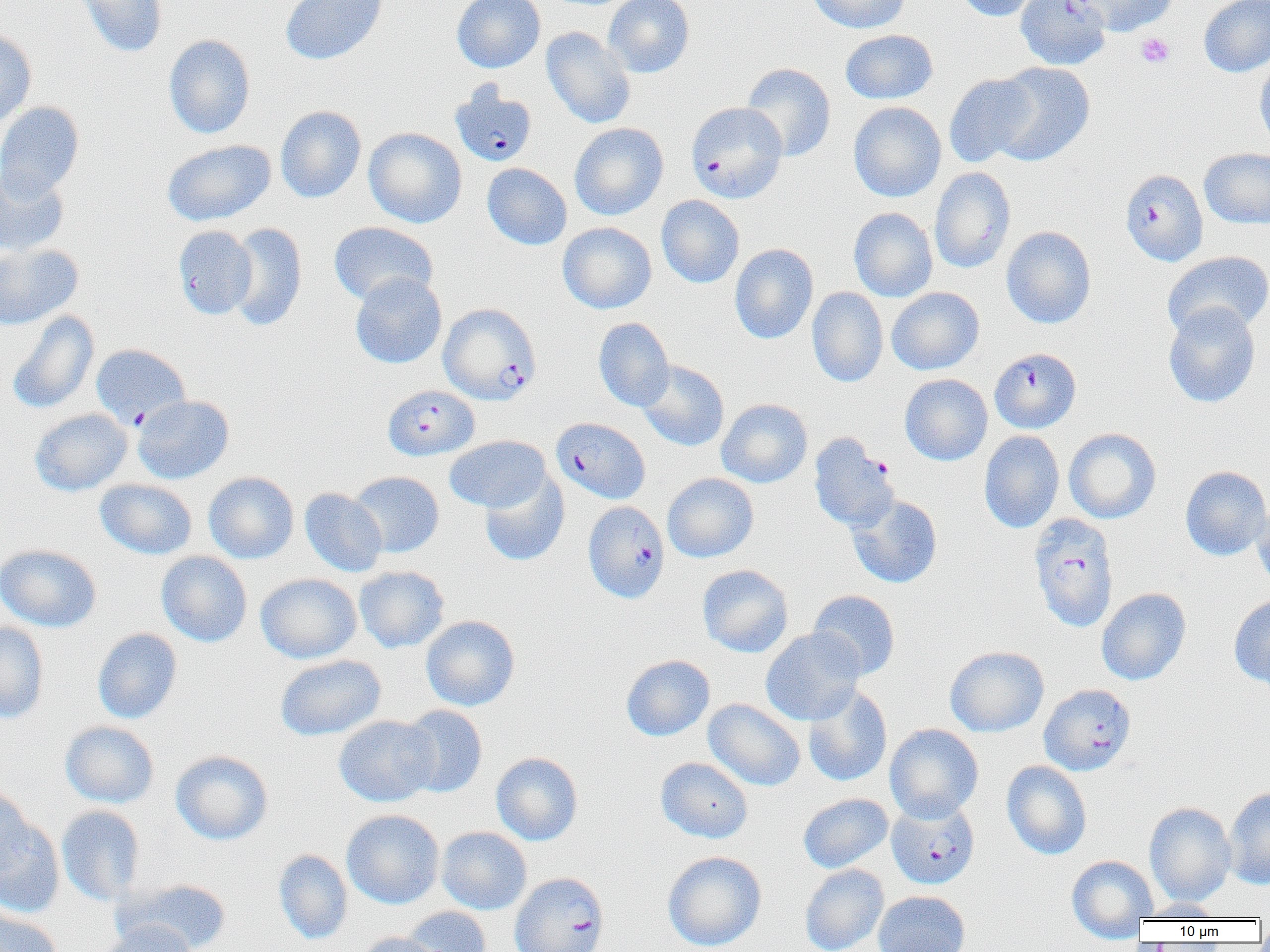

Summary:
  - Coordinate format: approximate bounding boxes as [x1, y1, x2, y2] in pixels
  - Uninfected red blood cell locations (subset): [76, 0, 167, 58], [279, 0, 389, 65], [452, 0, 545, 73], [604, 0, 694, 78], [808, 0, 911, 33], [953, 0, 1043, 21], [1071, 0, 1179, 36], [1199, 0, 1270, 77], [541, 26, 635, 129], [840, 29, 938, 104], [0, 30, 37, 127], [164, 34, 255, 139], [1255, 55, 1270, 151], [988, 62, 1095, 166], [741, 63, 836, 162], [944, 73, 1038, 167], [848, 102, 946, 202], [0, 103, 84, 199], [275, 105, 366, 203], [569, 122, 668, 220], [363, 127, 467, 228], [162, 139, 276, 226], [1199, 147, 1270, 229], [482, 163, 572, 250], [0, 166, 69, 256], [930, 166, 1016, 273], [656, 195, 745, 288], [848, 207, 937, 302], [328, 221, 438, 306], [557, 222, 656, 314], [227, 223, 307, 331], [173, 225, 257, 319], [1001, 225, 1096, 329], [0, 243, 83, 330], [729, 243, 818, 345], [1162, 251, 1270, 339], [350, 272, 447, 369], [807, 287, 888, 387], [886, 287, 984, 375], [1163, 302, 1260, 408], [7, 309, 100, 414], [594, 318, 675, 411], [637, 360, 729, 452], [899, 374, 993, 465], [132, 395, 234, 483], [716, 398, 812, 488], [29, 408, 132, 495], [1064, 428, 1161, 523], [979, 430, 1064, 533], [445, 435, 551, 513], [1180, 466, 1270, 560], [203, 471, 299, 564], [349, 471, 444, 558], [479, 471, 569, 567], [662, 473, 759, 562], [95, 478, 198, 560], [300, 488, 388, 577], [847, 494, 943, 588], [1252, 500, 1270, 593], [0, 544, 101, 632], [157, 551, 252, 647], [697, 564, 793, 657], [354, 566, 449, 653], [256, 573, 361, 663], [1096, 588, 1192, 686], [808, 590, 900, 681], [1229, 593, 1270, 689], [421, 615, 520, 711], [0, 621, 49, 724], [761, 627, 865, 725], [92, 628, 182, 724], [945, 645, 1049, 737], [274, 655, 386, 741], [621, 655, 714, 741], [803, 685, 892, 786], [703, 699, 805, 791], [397, 705, 488, 798], [333, 715, 438, 807], [59, 721, 159, 808], [884, 723, 983, 822], [170, 750, 273, 845], [491, 752, 583, 845], [655, 757, 753, 843], [1002, 761, 1092, 859], [0, 783, 34, 880], [1224, 786, 1270, 889], [798, 793, 893, 873], [1144, 801, 1236, 906], [56, 805, 145, 905], [341, 809, 444, 909], [0, 816, 65, 917], [436, 826, 532, 914], [273, 849, 353, 944], [662, 850, 767, 952], [1066, 854, 1157, 940], [800, 864, 888, 952], [115, 877, 232, 952], [873, 890, 971, 952], [1137, 899, 1226, 920], [400, 906, 492, 952], [0, 909, 63, 952], [95, 921, 198, 952], [356, 932, 444, 952]
  - Platelet locations: [1136, 33, 1175, 68]
  - Plasmodium falciparum-infected red blood cell locations (subset): [450, 83, 537, 167], [686, 102, 787, 203], [1120, 168, 1208, 266], [438, 303, 541, 405], [91, 343, 190, 428], [990, 348, 1080, 433], [382, 385, 480, 461], [551, 417, 649, 504], [583, 500, 670, 603], [1029, 513, 1119, 631], [1038, 683, 1136, 776], [887, 799, 980, 888], [509, 872, 609, 952]
  - Slide-level diagnosis: Plasmodium falciparum
  - Preparation: thin blood smear
  - Field of view: single
  - Magnification: 1000x
  - Image size: 1270×952 pixels
  - Modality: optical microscopy